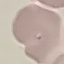
Result: no malaria parasites seen. Photographed with a smartphone camera at the microscope eyepiece. Cell patch, automatically extracted from a larger field of view and resized to 64 × 64 pixels. Giemsa stain. Thin blood film.